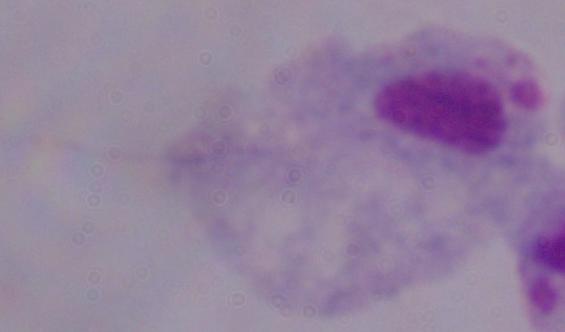 A trichomonad is seen. Micrograph. Captured at 1000x magnification.